Locate and identify every blood parasite.
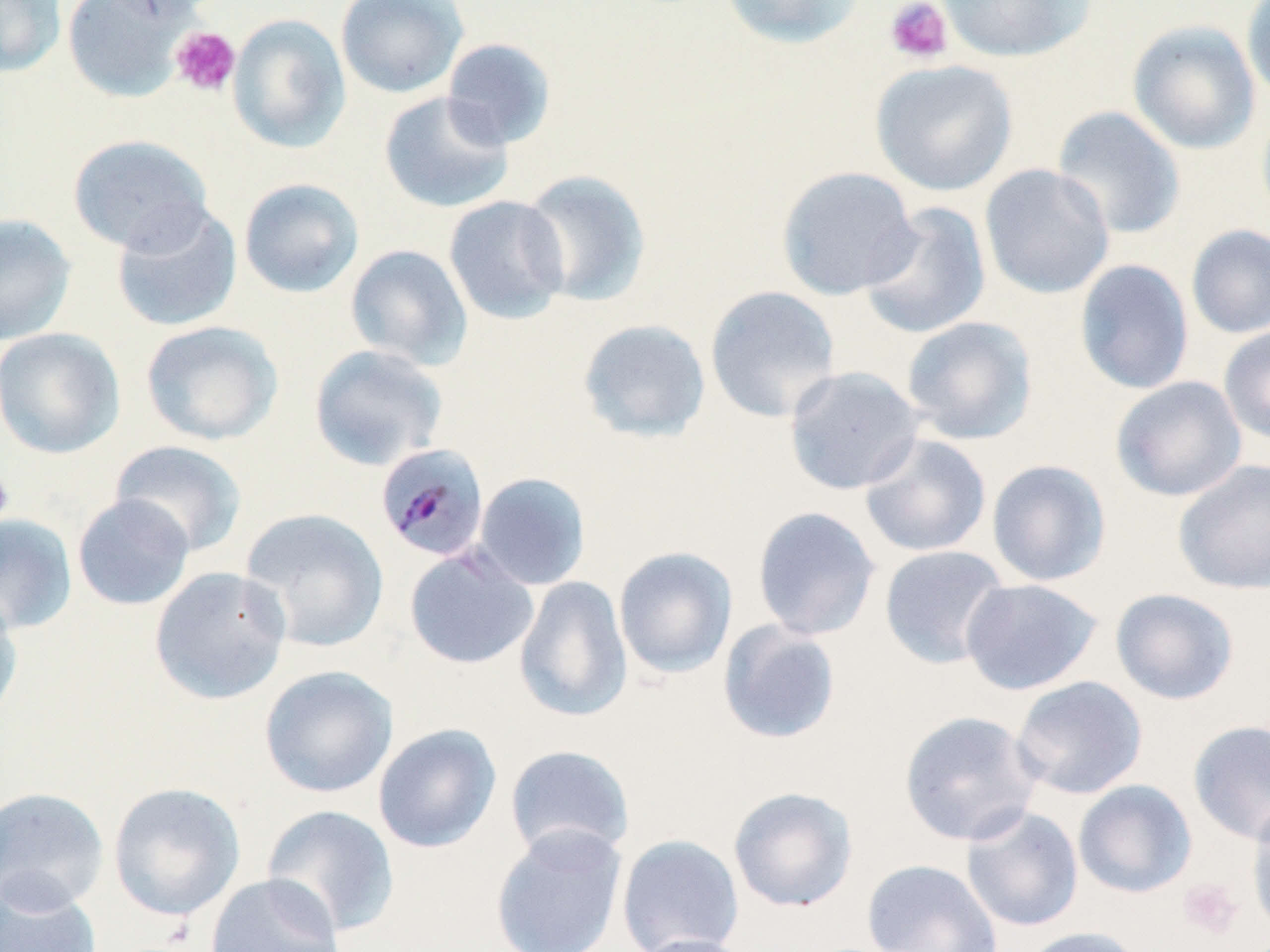
Approximate bounding boxes as named x1/y1/x2/y2 corners in pixels.
Plasmodium malariae-infected red blood cells: (x1=375, y1=442, x2=491, y2=563).
No Plasmodium falciparum, Plasmodium ovale, Plasmodium vivax, Babesia divergens, or Trypanosoma brucei observed.

Platelet locations: (x1=884, y1=0, x2=954, y2=65), (x1=169, y1=26, x2=240, y2=97), (x1=0, y1=467, x2=15, y2=527), (x1=1178, y1=878, x2=1244, y2=939). Uninfected red blood cell locations: (x1=0, y1=0, x2=67, y2=78), (x1=62, y1=0, x2=198, y2=103), (x1=92, y1=0, x2=217, y2=25), (x1=335, y1=0, x2=469, y2=99), (x1=719, y1=0, x2=867, y2=49), (x1=938, y1=0, x2=1096, y2=63), (x1=1241, y1=0, x2=1270, y2=108), (x1=227, y1=14, x2=351, y2=153), (x1=1127, y1=20, x2=1261, y2=155), (x1=441, y1=38, x2=557, y2=149), (x1=870, y1=59, x2=1019, y2=196), (x1=379, y1=91, x2=514, y2=214), (x1=1256, y1=101, x2=1270, y2=228), (x1=1051, y1=105, x2=1186, y2=240), (x1=67, y1=134, x2=213, y2=255), (x1=979, y1=163, x2=1115, y2=299), (x1=776, y1=166, x2=920, y2=300), (x1=518, y1=168, x2=652, y2=308), (x1=238, y1=177, x2=365, y2=299), (x1=443, y1=195, x2=570, y2=325), (x1=111, y1=201, x2=243, y2=333), (x1=858, y1=201, x2=991, y2=340), (x1=0, y1=213, x2=77, y2=346), (x1=1185, y1=224, x2=1270, y2=339), (x1=345, y1=243, x2=473, y2=370), (x1=1074, y1=258, x2=1194, y2=395), (x1=704, y1=285, x2=841, y2=423), (x1=901, y1=316, x2=1039, y2=445), (x1=577, y1=319, x2=711, y2=444), (x1=140, y1=320, x2=283, y2=446), (x1=1218, y1=325, x2=1270, y2=444), (x1=0, y1=327, x2=125, y2=459), (x1=308, y1=344, x2=449, y2=471), (x1=783, y1=366, x2=926, y2=495), (x1=1110, y1=375, x2=1247, y2=503), (x1=859, y1=433, x2=992, y2=557), (x1=109, y1=439, x2=247, y2=557), (x1=1172, y1=458, x2=1270, y2=596), (x1=986, y1=459, x2=1112, y2=587), (x1=473, y1=472, x2=591, y2=590), (x1=72, y1=494, x2=195, y2=611), (x1=751, y1=505, x2=881, y2=641), (x1=240, y1=508, x2=390, y2=653), (x1=0, y1=513, x2=78, y2=635), (x1=878, y1=544, x2=1011, y2=669), (x1=404, y1=546, x2=539, y2=670), (x1=613, y1=546, x2=738, y2=680), (x1=148, y1=566, x2=291, y2=706), (x1=513, y1=575, x2=633, y2=724), (x1=960, y1=578, x2=1103, y2=696), (x1=1110, y1=588, x2=1239, y2=705), (x1=0, y1=589, x2=24, y2=729), (x1=717, y1=620, x2=842, y2=745), (x1=259, y1=665, x2=397, y2=799), (x1=1010, y1=675, x2=1149, y2=799), (x1=898, y1=710, x2=1043, y2=847), (x1=1187, y1=719, x2=1270, y2=845), (x1=373, y1=723, x2=502, y2=853), (x1=503, y1=744, x2=636, y2=862), (x1=1073, y1=779, x2=1197, y2=898), (x1=108, y1=782, x2=246, y2=922), (x1=0, y1=786, x2=110, y2=913), (x1=727, y1=786, x2=859, y2=913), (x1=1245, y1=801, x2=1270, y2=937), (x1=261, y1=804, x2=400, y2=939), (x1=961, y1=805, x2=1084, y2=932), (x1=489, y1=824, x2=629, y2=952), (x1=616, y1=834, x2=745, y2=952), (x1=861, y1=858, x2=1003, y2=952), (x1=204, y1=873, x2=344, y2=952), (x1=0, y1=875, x2=102, y2=952), (x1=1018, y1=926, x2=1143, y2=952), (x1=629, y1=933, x2=758, y2=952). Slide-level diagnosis: Plasmodium malariae. May-Grünwald-Giemsa stain. Single field of view. Optical microscopy. Image is 1270×952 pixels. Captured at 1000x magnification. Thin blood film.